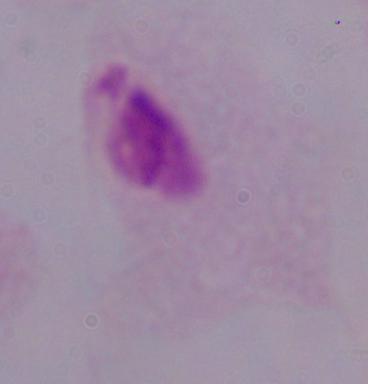
Summary:
  - Modality: photomicrograph
  - Magnification: 1000x
  - Identification: trichomonad